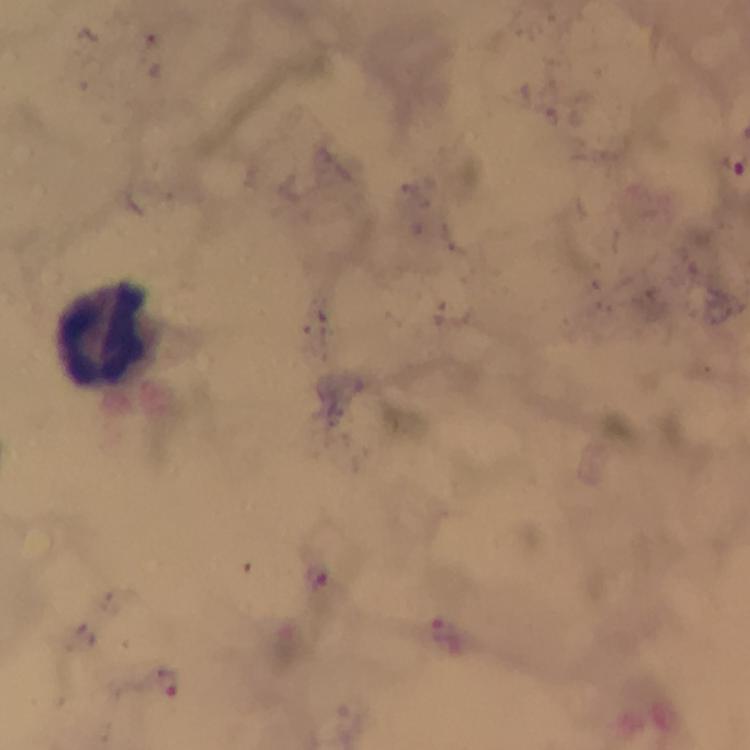 Approximate centers as [x, y] in pixels. Plasmodium parasite locations: [317, 576], [446, 635], [167, 684]. Leukocyte locations: [103, 333]. 100x magnification. Thick smear. Giemsa stain. Immersion oil was used. Photographed through the microscope with a smartphone camera. Image is 750×750 pixels. Cropped region of a single field of view. From a malaria diagnostic workup.